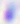
Toxoplasma gondii is shown. Captured at 400x magnification. Micrograph.